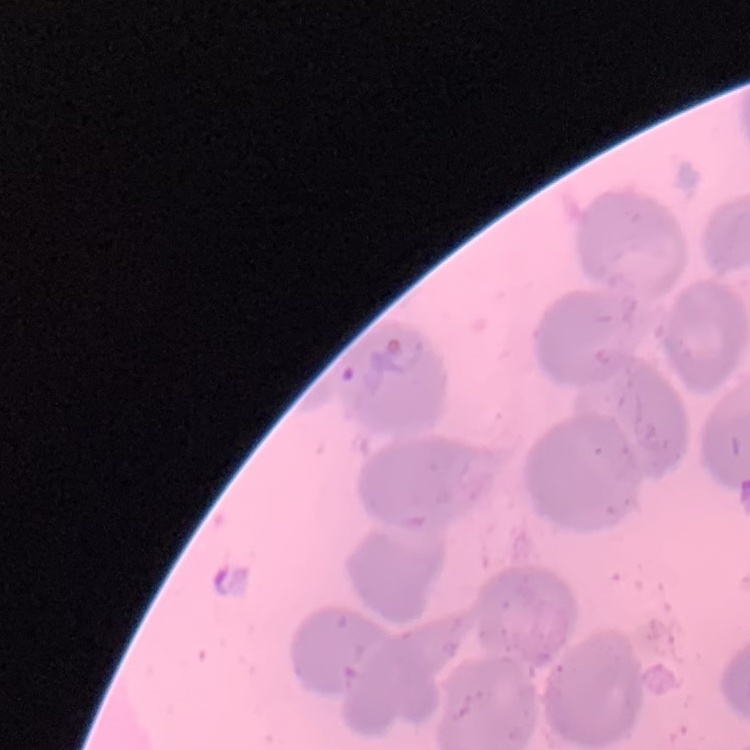
Summary:
  - Erythrocyte morphology: no rouleaux formation
  - Stain: Field's or Giemsa
  - Preparation: thin blood smear
  - Image type: one tile cut from a larger photomicrograph